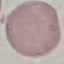
Malaria status: uninfected. Cell patch, automatically extracted from a larger field of view and resized to 64 × 64 pixels. Thin blood film. Acquired by smartphone through the microscope eyepiece. Giemsa-stained preparation.